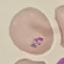

Malaria status: parasitized. Cell patch, automatically extracted from a larger field of view and resized to 64 × 64 pixels. Thin blood smear. Acquired by smartphone through the microscope eyepiece. Giemsa-stained preparation.